Report the malaria status of this cell.
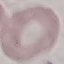
Uninfected.

Thin smear of blood. Photographed with a smartphone camera at the microscope eyepiece. Automatically extracted cell patch, resized to 64 × 64 pixels. Giemsa stain.